Assess the morphology of the red blood cells.
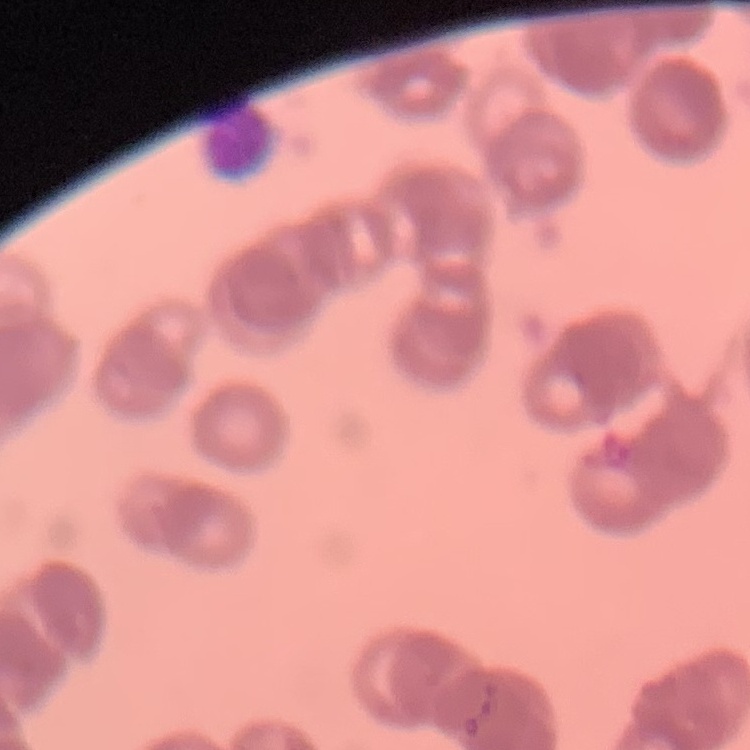
They show rouleaux formation.

Thin peripheral smear. One tile cut from a larger photomicrograph. Stained with either Field's or Giemsa.